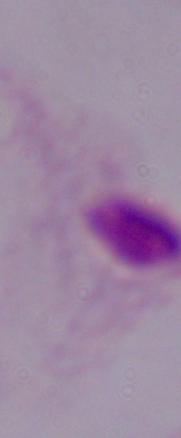

Summary:
  - Identification: trichomonad
  - Modality: micrograph
  - Magnification: 1000x